Point out each Plasmodium parasite.
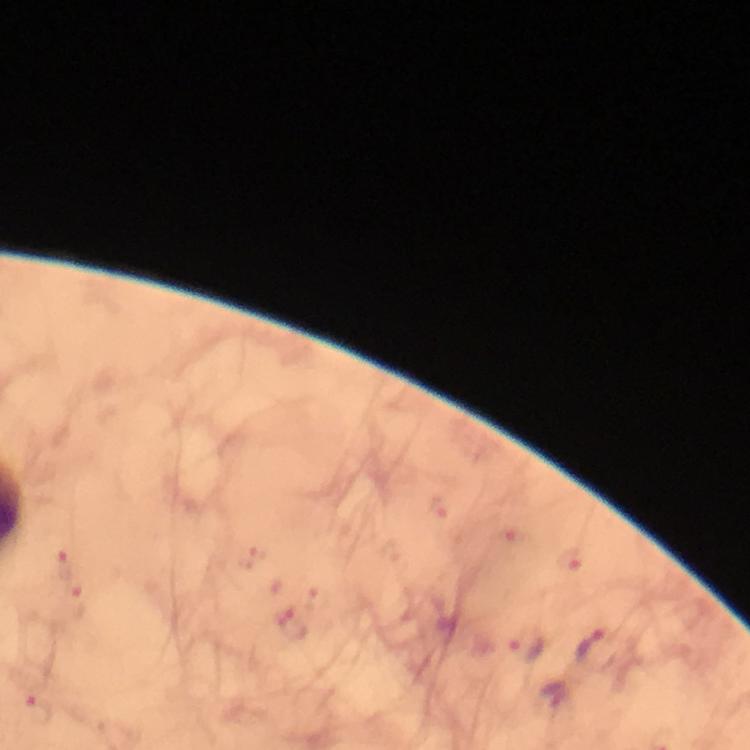
Approximate centers as {x, y} in pixels.
Plasmodium parasites: {76, 602}, {528, 648}, {598, 649}, {555, 697}.

Summary:
  - Context: from a malaria diagnostic workup
  - Preparation: thick blood film
  - Cropped from: a single field of view
  - Capture: smartphone camera through the microscope
  - Magnification: 100x
  - Immersion oil: used
  - Stain: Giemsa
  - Image size: 750×750 pixels